Give the extent of all Plasmodium vivax-infected red blood cells.
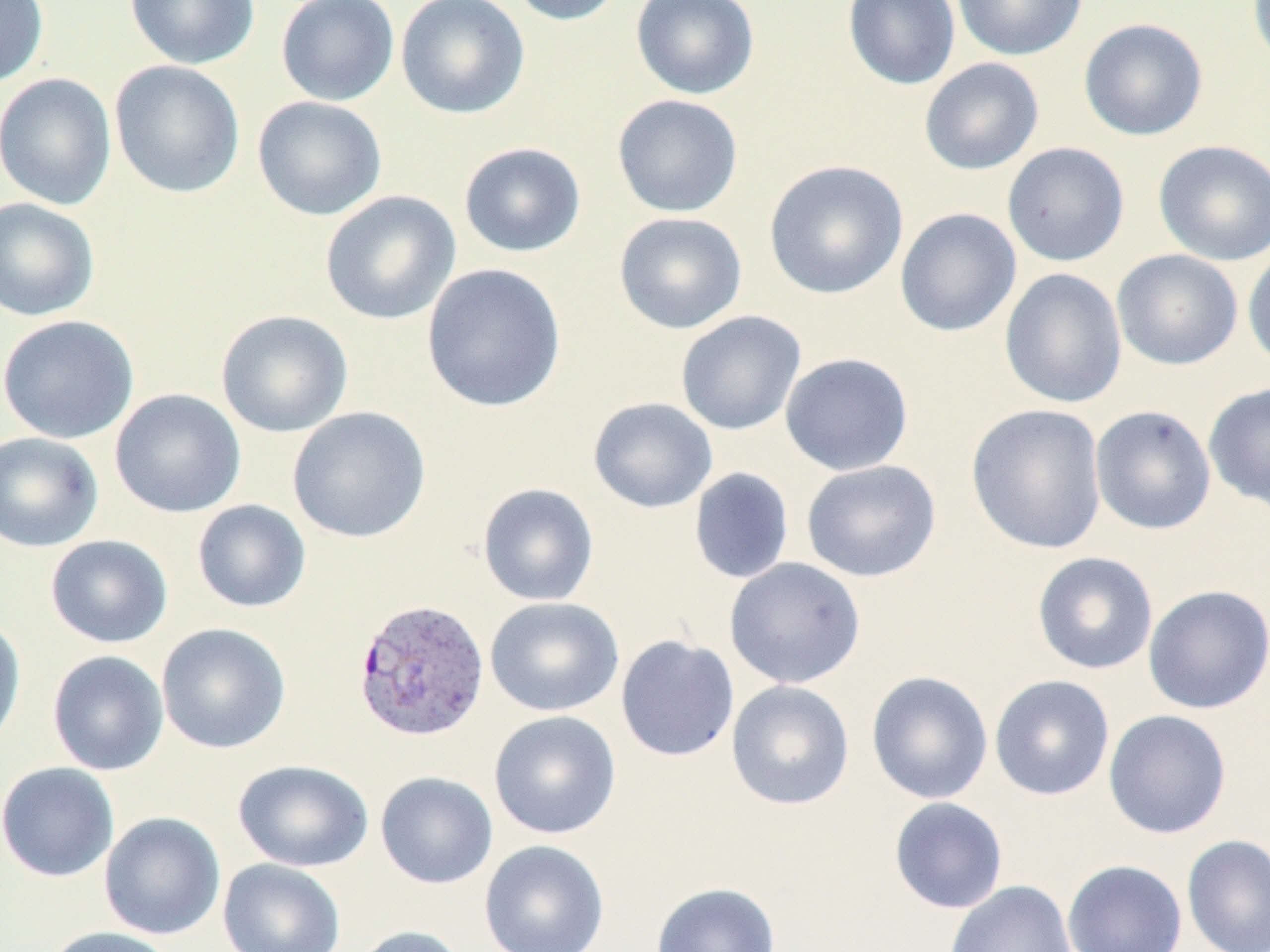

Approximate bounding boxes as (x1,y1)-(x2,y2) corner pairs in pixels.
Plasmodium vivax-infected red blood cells: (352,596)-(491,743).

Uninfected red blood cell locations: (0,0)-(49,87), (124,0)-(261,70), (276,0)-(400,107), (396,0)-(530,120), (507,0)-(626,26), (630,0)-(760,100), (843,0)-(961,90), (952,0)-(1087,61), (1247,0)-(1270,71), (1078,17)-(1208,140), (919,58)-(1044,175), (110,60)-(245,198), (0,73)-(116,209), (612,94)-(744,218), (252,95)-(387,220), (1153,139)-(1270,266), (458,142)-(586,258), (1002,142)-(1130,267), (763,160)-(909,300), (320,191)-(461,325), (0,197)-(100,321), (895,208)-(1021,337), (613,212)-(747,334), (1242,243)-(1270,373), (1112,249)-(1243,370), (421,263)-(567,413), (999,268)-(1127,409), (216,309)-(353,438), (675,311)-(806,436), (0,314)-(139,444), (780,352)-(914,476), (1203,382)-(1270,512), (110,388)-(246,518), (588,397)-(718,513), (966,403)-(1107,555), (1090,405)-(1217,536), (287,406)-(431,543), (0,431)-(103,552), (801,459)-(942,582), (688,467)-(795,584), (477,482)-(599,606), (192,499)-(311,613), (45,534)-(173,648), (1031,551)-(1158,676), (724,557)-(866,690), (1142,584)-(1270,715), (484,596)-(624,717), (0,615)-(27,753), (156,623)-(291,754), (615,634)-(740,762), (47,650)-(169,776), (866,670)-(994,804), (988,674)-(1115,801), (726,680)-(855,810), (1103,709)-(1233,839), (488,710)-(622,840), (233,759)-(375,872), (0,761)-(119,882), (375,771)-(498,889), (888,797)-(1008,914), (99,811)-(226,940), (1181,833)-(1270,952), (479,839)-(610,952), (218,858)-(346,952), (1062,859)-(1187,952), (944,880)-(1077,952), (650,882)-(781,952), (350,925)-(467,952), (44,926)-(176,952). Slide-level diagnosis: Plasmodium vivax. Captured at 1000x magnification. One field of a larger specimen. Thin blood smear. Image is 1270×952 pixels. Light microscopy. May-Grünwald-Giemsa stain.